Identify the parasite.
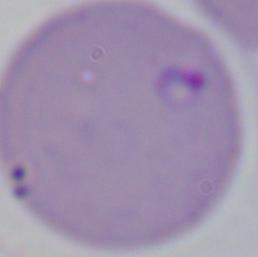
Babesia.

Summary:
  - Modality: photomicrograph
  - Magnification: 1000x